Comment on the morphology of the red blood cells.
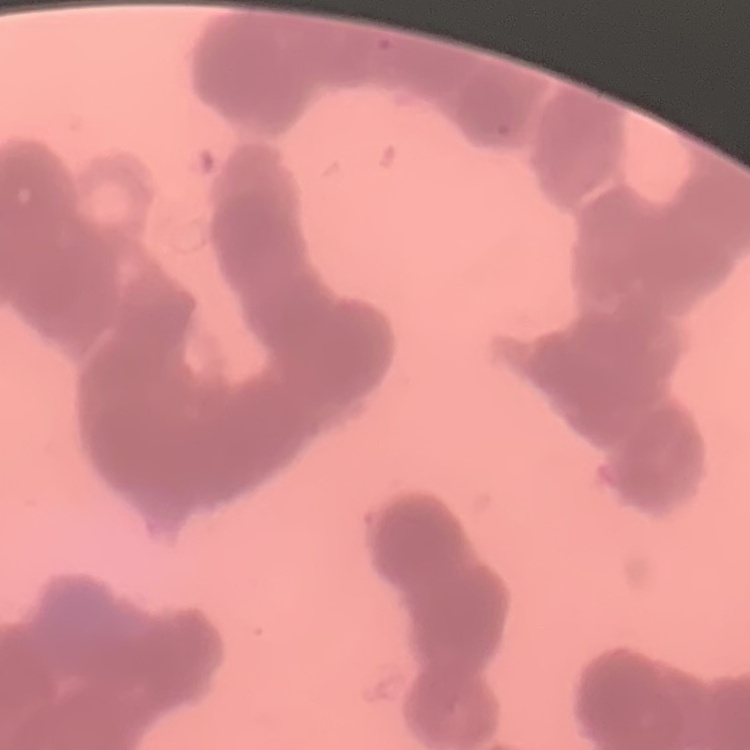
Rouleaux formation.

Stained with either Field's or Giemsa. Thin blood film. Square crop of a larger photomicrograph.